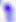

{
  "magnification": "400x",
  "modality": "micrograph",
  "identification": "Toxoplasma gondii"
}